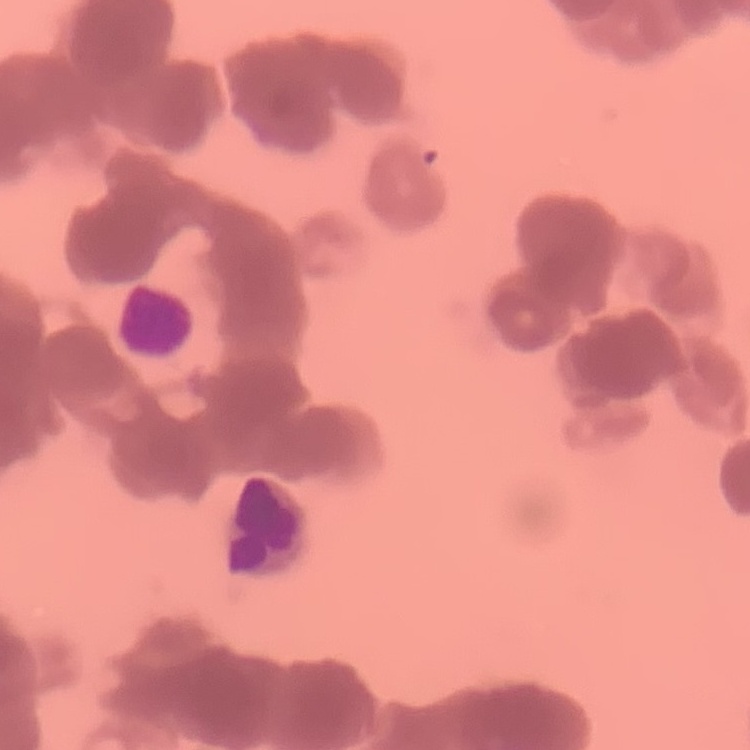

erythrocyte morphology = rouleaux formation
preparation = thin blood film
stain = Field's or Giemsa
image type = square crop of a larger photomicrograph